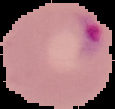
Summary:
  - Preparation: thin blood smear
  - Image type: segmented cell region on a black background
  - Image size: 115×109 pixels
  - Result: malaria parasites detected